State which parasite is depicted.
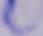
This is a trypanosome.

Micrograph. 1000x magnification.